Assess this cell for malaria.
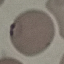
It is parasitized.

capture = smartphone through the microscope eyepiece
image type = automatically extracted cell patch, resized to 64 × 64 pixels
preparation = thin blood smear
stain = Giemsa